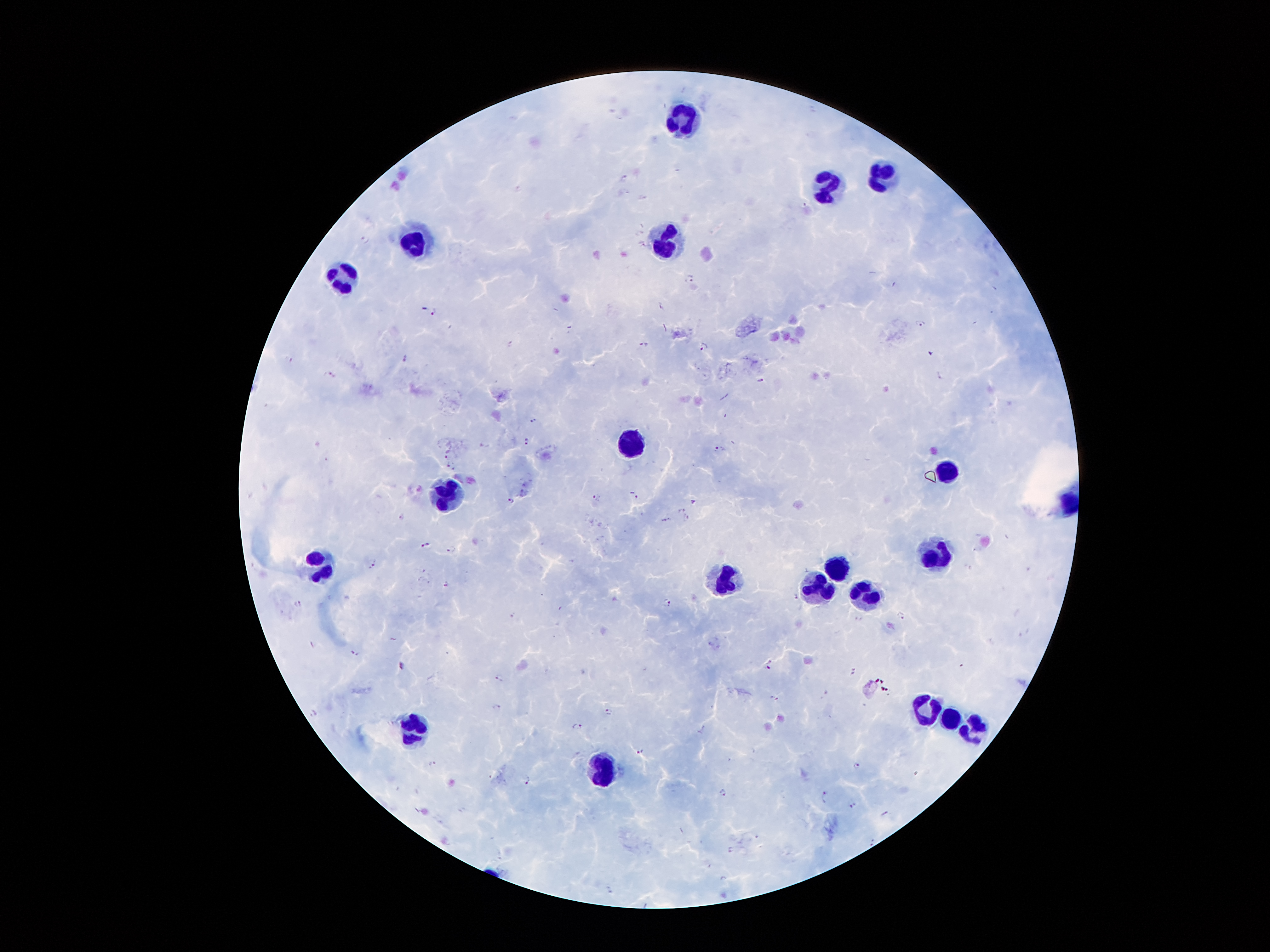
coordinate format = approximate centers as {x, y} in pixels
leukocyte locations = {687, 122}, {884, 173}, {830, 186}, {420, 238}, {668, 243}, {344, 280}, {631, 444}, {947, 470}, {449, 495}, {937, 555}, {320, 563}, {838, 565}, {727, 580}, {820, 586}, {864, 595}, {929, 709}, {952, 716}, {416, 725}, {977, 728}, {606, 768}
Plasmodium parasite locations = {623, 179}, {641, 198}, {643, 243}, {689, 278}, {432, 311}, {919, 323}, {643, 345}, {704, 346}, {930, 352}, {404, 358}, {329, 374}, {940, 374}, {759, 379}, {534, 420}, {526, 441}, {485, 443}, {719, 449}, {449, 453}, {451, 464}, {633, 494}, {595, 498}, {511, 500}, {692, 502}, {681, 508}, {403, 516}, {685, 518}, {666, 520}, {426, 544}, {450, 549}, {372, 562}, {446, 584}, {666, 602}, {298, 605}, {513, 614}, {401, 664}, {768, 664}, {499, 678}, {496, 707}, {608, 712}, {313, 713}, {576, 726}, {640, 749}, {432, 763}, {856, 765}, {525, 778}, {723, 792}, {826, 795}, {853, 804}, {884, 814}, {730, 849}
preparation = thick blood smear
image size = 1270×952 pixels
field of view = single
patient malaria status = infected with Plasmodium falciparum
capture = smartphone camera through the microscope eyepiece
magnification = 100x
stain = Giemsa